Comment on the morphology of the erythrocytes.
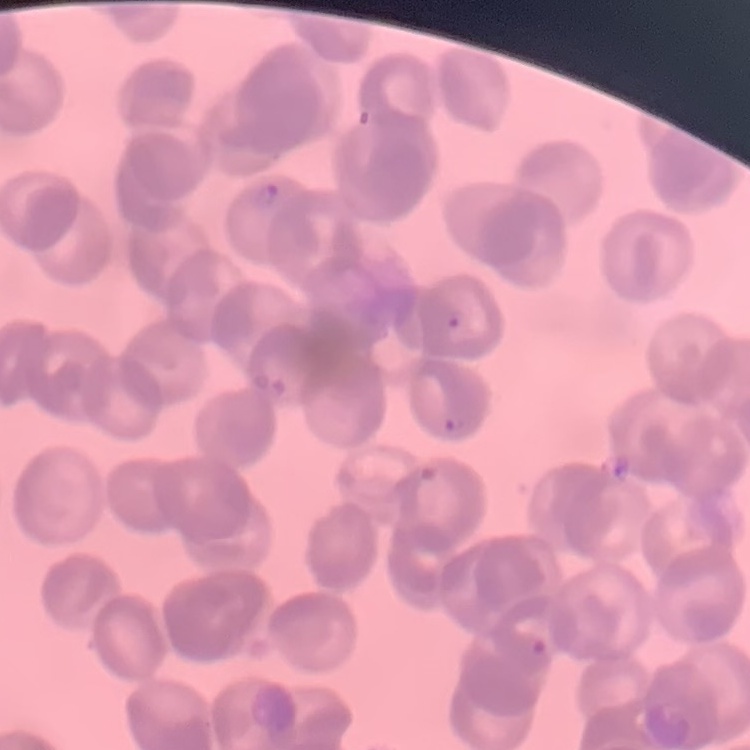
They show rouleaux formation.

Field's or Giemsa stain. Square crop of a larger photomicrograph. Thin blood smear.